Report the malaria status of this cell.
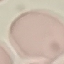
It is uninfected.

Summary:
  - Stain: Giemsa
  - Capture: smartphone through the microscope eyepiece
  - Preparation: thin blood smear
  - Image type: automatically extracted cell patch, resized to 64 × 64 pixels